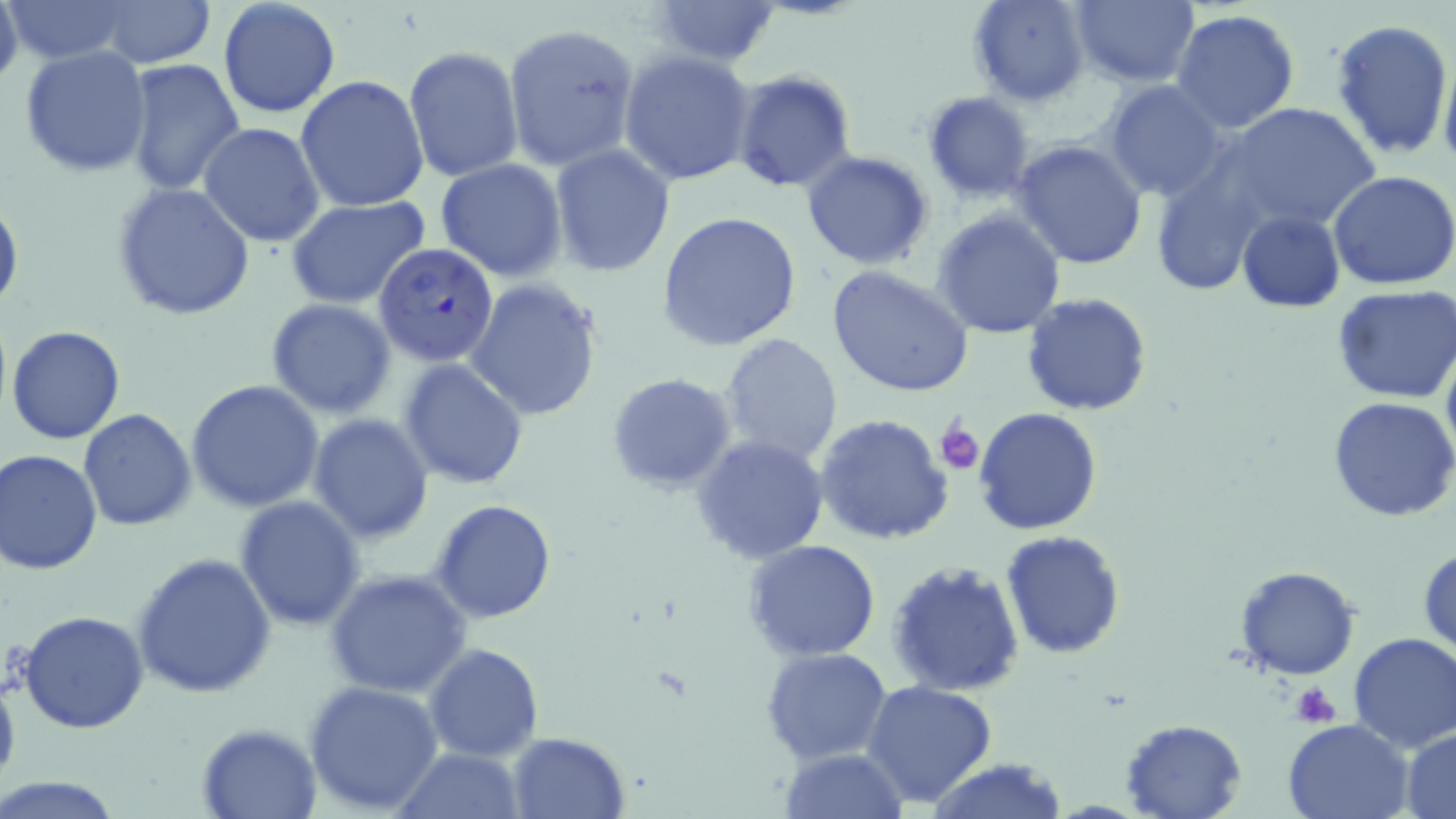
Summary:
  - Coordinate format: approximate bounding boxes as (x1, y1, x2, y2) in pixels
  - Platelet locations: (937, 418, 984, 476), (1291, 683, 1343, 727)
  - Plasmodium falciparum-infected red blood cell locations: (373, 242, 501, 367)
  - Uninfected red blood cell locations: (0, 0, 23, 90), (2, 0, 142, 65), (217, 0, 340, 119), (653, 0, 778, 68), (969, 0, 1089, 106), (1071, 0, 1201, 86), (94, 2, 214, 69), (1170, 9, 1301, 135), (1331, 17, 1454, 160), (502, 21, 638, 172), (19, 45, 152, 178), (404, 46, 524, 182), (618, 48, 757, 187), (1439, 49, 1456, 178), (122, 58, 246, 197), (730, 68, 857, 193), (296, 76, 430, 213), (1102, 81, 1229, 201), (923, 93, 1035, 203), (1223, 102, 1382, 235), (199, 121, 325, 247), (1010, 138, 1149, 272), (549, 145, 676, 279), (801, 151, 934, 271), (436, 158, 568, 281), (1328, 171, 1456, 292), (112, 183, 258, 321), (285, 196, 430, 310), (0, 198, 23, 319), (932, 208, 1066, 339), (1237, 210, 1345, 312), (657, 211, 803, 351), (828, 265, 974, 399), (463, 277, 604, 421), (1333, 287, 1456, 403), (1021, 293, 1152, 415), (265, 299, 397, 420), (7, 325, 126, 444), (718, 332, 844, 466), (1441, 338, 1456, 468), (397, 359, 529, 488), (607, 374, 737, 493), (185, 378, 324, 512), (1329, 397, 1456, 521), (975, 406, 1104, 536), (78, 409, 197, 531), (308, 412, 434, 543), (814, 413, 955, 544), (691, 435, 830, 563), (0, 450, 103, 575), (234, 494, 366, 631), (429, 498, 558, 623), (1000, 530, 1126, 660), (745, 540, 881, 661), (1418, 546, 1455, 658), (131, 552, 277, 698), (886, 560, 1026, 697), (1233, 564, 1362, 680), (325, 568, 474, 700), (19, 610, 150, 734), (1347, 632, 1456, 751), (423, 643, 544, 762), (761, 647, 893, 765), (0, 671, 21, 793), (862, 678, 999, 809), (303, 681, 445, 813), (1121, 717, 1249, 819), (1283, 718, 1413, 819), (195, 721, 325, 818), (1402, 729, 1456, 816), (507, 731, 628, 817), (396, 746, 526, 818), (779, 746, 910, 818), (930, 759, 1068, 819), (0, 773, 125, 817)
  - Slide-level diagnosis: Plasmodium falciparum
  - Field of view: single
  - Image size: 1456×819 pixels
  - Preparation: thin blood film
  - Magnification: 1000x
  - Modality: optical microscopy
  - Stain: May-Grünwald-Giemsa